Classify this cell by malaria status.
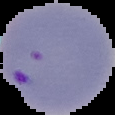
Parasitized.

preparation: thin blood film
image_size: 115×115 pixels
image_type: segmented cell region with the area outside set to black